Locate every leukocyte (white blood cell).
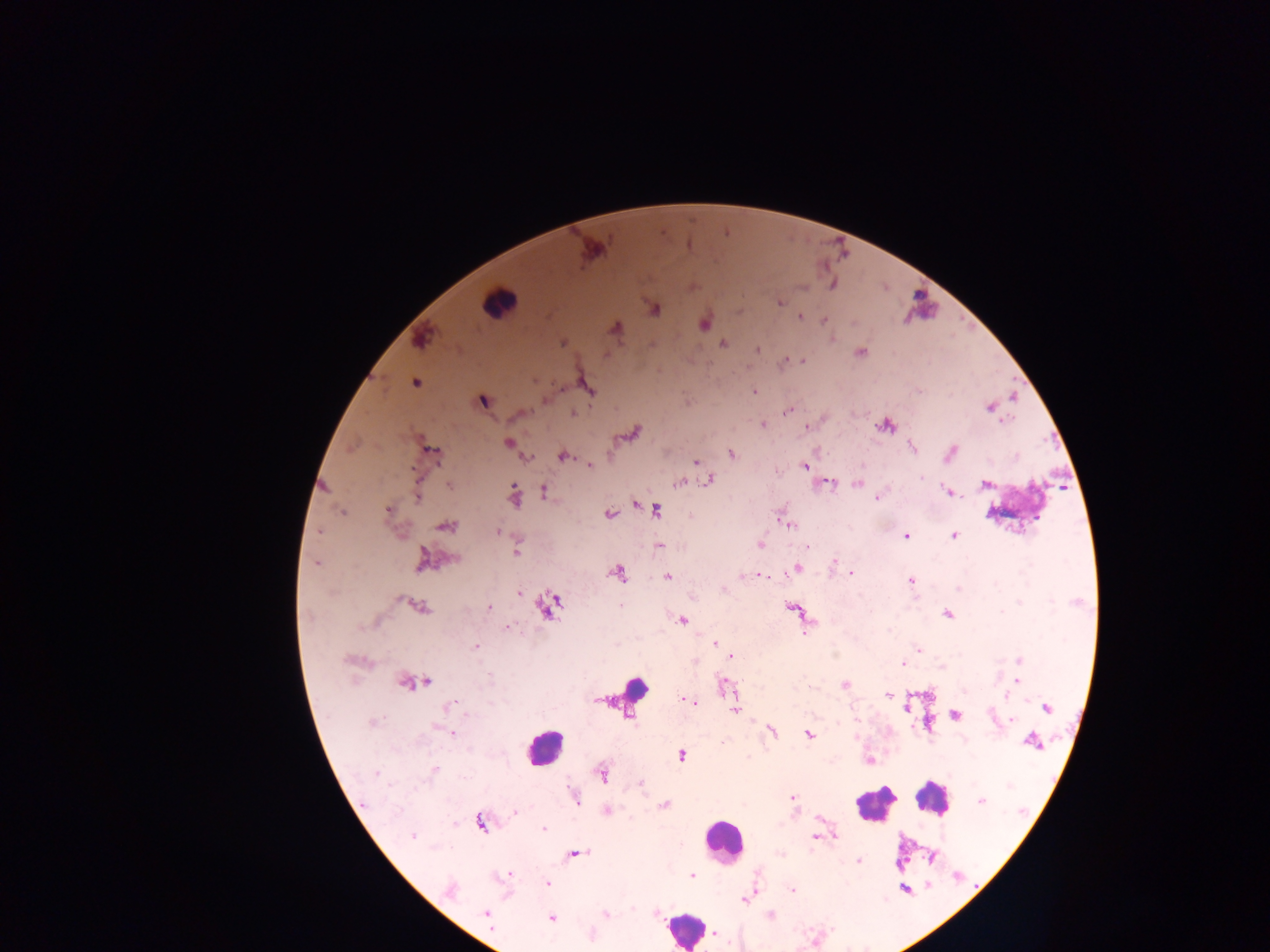
Approximate centers as x y in pixels.
Leukocytes: 498 303; 634 688; 544 746; 932 798; 874 804; 722 840; 683 928.

Summary:
  - Plasmodium parasite locations: 780 303; 654 308; 800 316; 824 320; 704 324; 615 328; 420 339; 563 343; 722 343; 757 349; 860 353; 784 361; 804 361; 534 380; 416 383; 587 386; 755 390; 483 401; 989 407; 786 412; 573 413; 763 425; 885 425; 806 427; 632 434; 508 442; 911 446; 432 451; 950 453; 731 454; 563 456; 527 458; 695 462; 589 465; 805 467; 922 478; 708 480; 678 483; 449 484; 857 484; 985 484; 544 492; 948 492; 418 496; 513 496; 876 498; 636 505; 388 509; 656 510; 342 512; 609 514; 446 525; 789 526; 319 532; 498 532; 907 536; 954 536; 759 546; 808 547; 517 553; 422 558; 452 559; 835 560; 317 563; 797 568; 851 573; 618 574; 761 575; 743 576; 667 577; 911 581; 959 588; 518 594; 1020 603; 620 605; 548 606; 420 607; 489 608; 793 610; 1002 612; 948 614; 683 620; 508 627; 806 631; 715 644; 476 646; 918 650; 732 657; 1019 660; 903 664; 490 678; 1016 681; 425 682; 404 684; 845 684; 965 691; 888 696; 1008 696; 689 700; 448 705; 1046 707; 735 710; 955 715; 1011 720; 372 721; 439 729; 772 731; 449 733; 808 734; 1032 742; 722 743; 681 755; 869 761; 434 769; 376 772; 602 774; 641 784; 793 797; 575 798; 981 801; 665 805; 515 811; 606 811; 480 822; 544 828; 413 836; 815 837; 577 854; 859 861; 506 875; 692 876; 548 883; 450 890; 793 890; 744 899; 605 913; 486 914; 771 915; 551 919; 714 933
  - Capture: mobile-phone photograph through a microscope
  - Field of view: single
  - Country: Ghana
  - Preparation: thick blood film
  - Image size: 1270×952 pixels